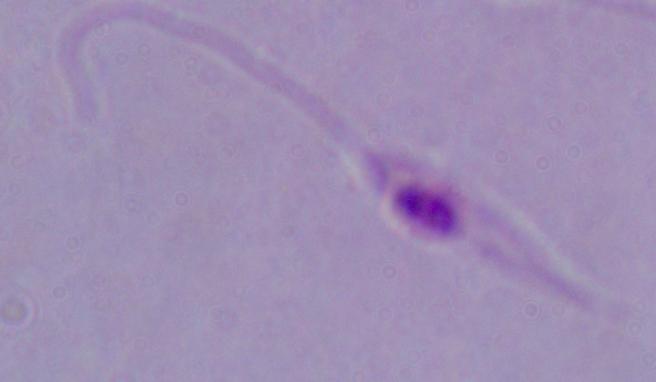

Summary:
  - Modality: micrograph
  - Magnification: 1000x
  - Identification: Leishmania